Locate and identify every blood parasite.
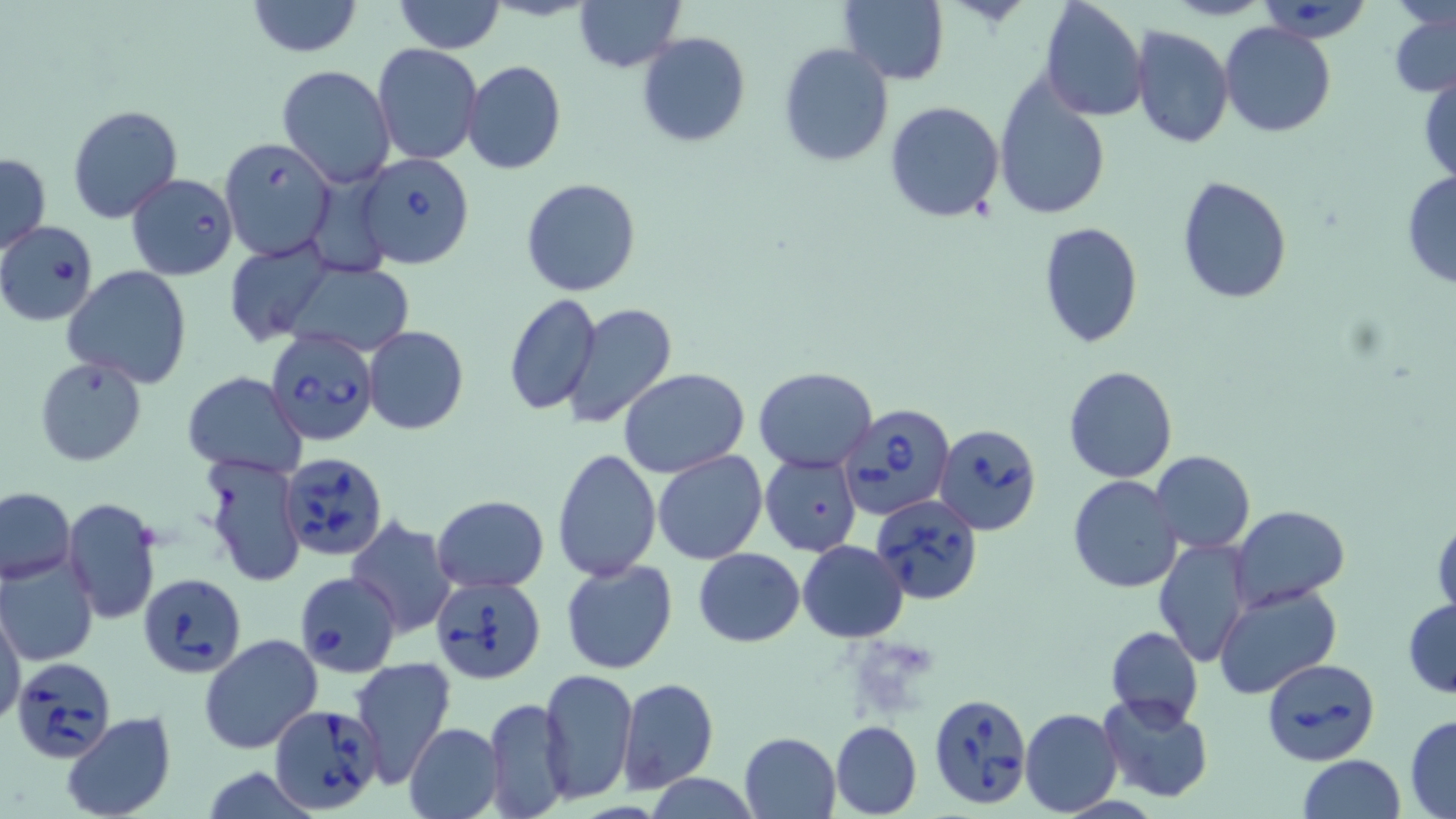

Approximate bounding boxes as (x1, y1, x2, y2) in pixels.
Babesia divergens-infected red blood cells: (1259, 1, 1376, 44), (219, 137, 336, 260), (355, 153, 474, 268), (125, 171, 236, 280), (0, 221, 99, 325), (265, 328, 378, 446), (838, 404, 957, 519), (934, 424, 1042, 536), (282, 451, 388, 561), (871, 493, 984, 604), (296, 565, 405, 675), (138, 572, 245, 676), (432, 576, 547, 684), (1260, 656, 1380, 766), (10, 657, 117, 765), (927, 691, 1033, 810), (269, 704, 385, 816).
No Plasmodium falciparum, Plasmodium ovale, Plasmodium malariae, Plasmodium vivax, or Trypanosoma brucei observed.

slide_level_diagnosis: Babesia divergens
uninfected_red_blood_cell_locations: 'approximate bounding boxes as (x1, y1, x2, y2) in pixels: (245, 0, 364, 56), (393, 0, 506, 54), (573, 0, 685, 72), (1038, 0, 1148, 121), (1164, 0, 1271, 21), (837, 1, 950, 85), (1389, 11, 1456, 97), (1220, 23, 1336, 138), (1129, 25, 1236, 148), (637, 32, 750, 148), (778, 41, 893, 167), (372, 44, 484, 165), (462, 60, 567, 176), (277, 64, 395, 186), (1418, 71, 1456, 187), (992, 74, 1111, 221), (883, 100, 1006, 223), (67, 104, 182, 223), (0, 152, 50, 255), (1401, 173, 1456, 289), (1176, 175, 1292, 303), (520, 178, 641, 297), (1037, 221, 1144, 349), (225, 238, 338, 345), (282, 261, 413, 356), (64, 267, 191, 388), (501, 292, 601, 415), (562, 301, 677, 429), (363, 325, 468, 434), (34, 356, 147, 465), (1064, 364, 1178, 483), (619, 367, 750, 477), (753, 367, 876, 473), (183, 371, 307, 476), (552, 448, 662, 582), (1151, 450, 1255, 553), (653, 451, 769, 565), (200, 454, 304, 588), (760, 456, 861, 555), (1068, 475, 1182, 592), (0, 488, 76, 583), (432, 494, 549, 594), (63, 498, 163, 625), (1232, 505, 1350, 609), (1431, 512, 1455, 624), (344, 517, 457, 639), (1153, 538, 1253, 667), (797, 541, 910, 641), (693, 547, 806, 646), (0, 554, 99, 666), (560, 559, 677, 675), (1213, 581, 1343, 702), (1403, 598, 1456, 699), (1, 606, 26, 729), (1104, 626, 1203, 728), (199, 634, 324, 754), (351, 657, 456, 785), (540, 669, 637, 803), (617, 677, 719, 793), (1098, 693, 1212, 803), (482, 698, 572, 819), (1020, 707, 1122, 815), (61, 712, 177, 819), (1405, 713, 1456, 817), (831, 720, 923, 818), (403, 722, 504, 819), (739, 731, 840, 817), (1298, 755, 1404, 819), (643, 775, 763, 816)'
preparation: thin blood film
magnification: 1000x
image_size: 1456×819 pixels
modality: optical microscopy
stain: May-Grünwald-Giemsa
field_of_view: single